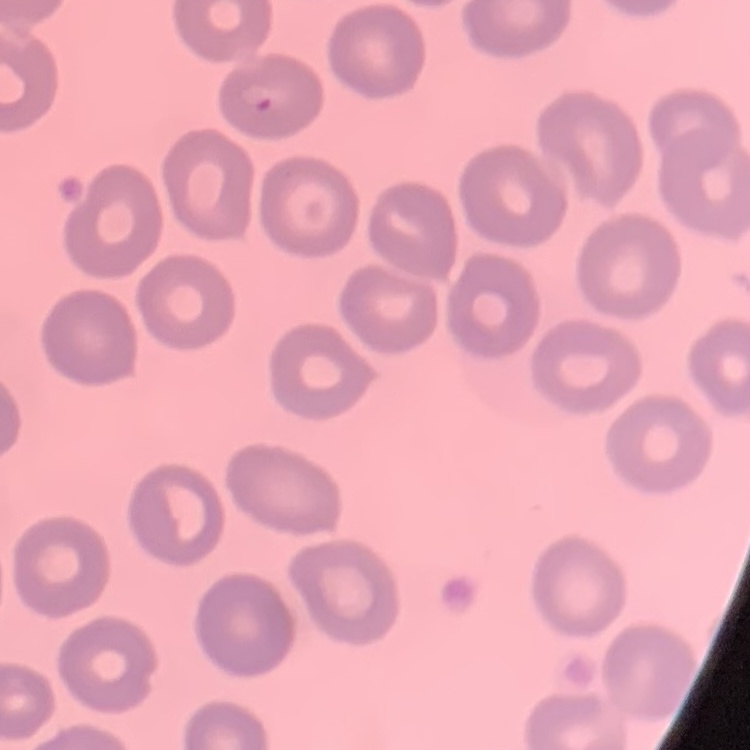

Summary:
  - Erythrocyte morphology: no rouleaux formation
  - Preparation: thin blood film
  - Image type: one tile cut from a larger photomicrograph
  - Stain: Field's or Giemsa